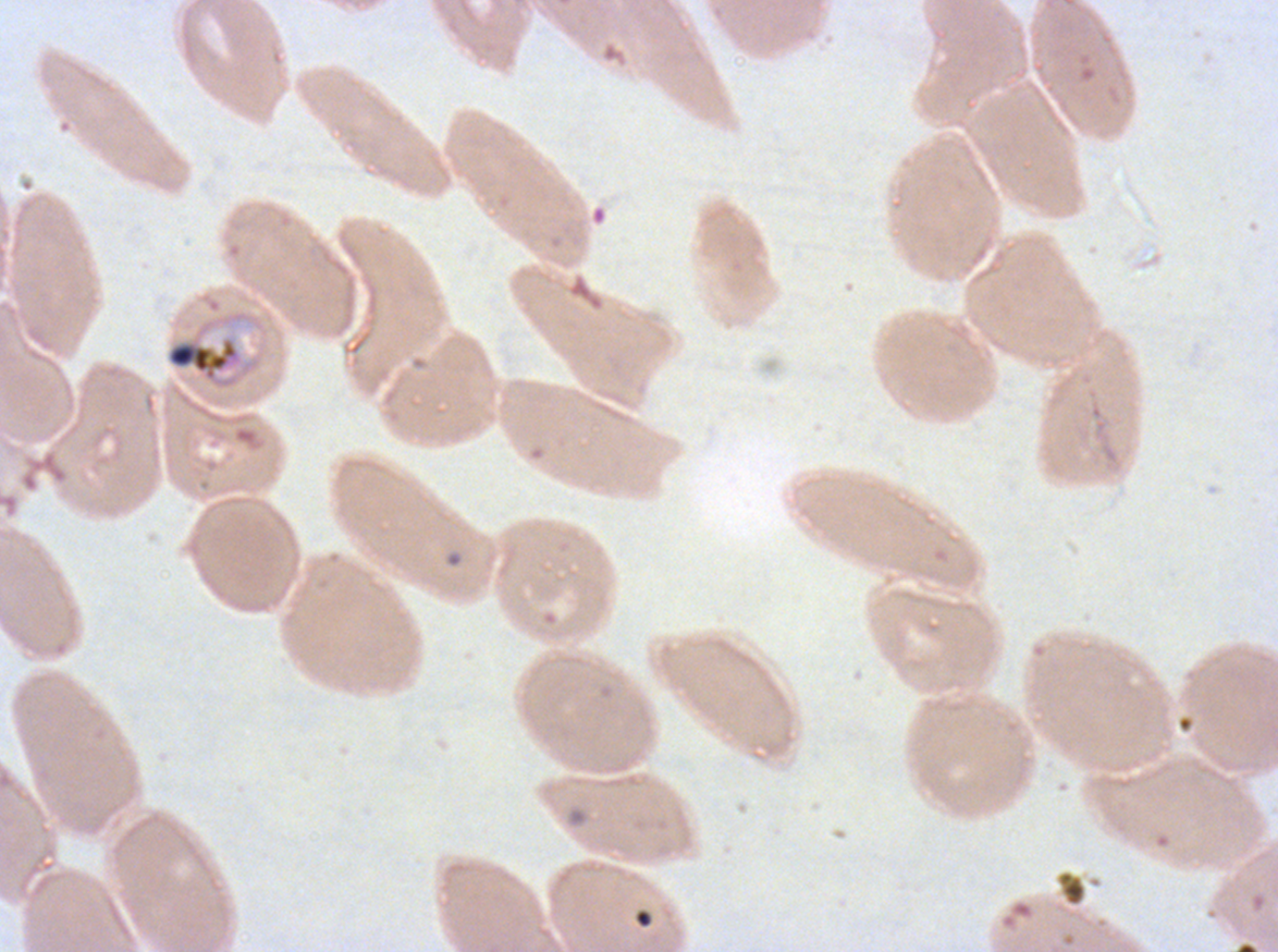
notation = approximate bounding boxes as {x1, y1, x2, y2} in pixels
mid trophozoite locations = {165, 309, 261, 391}
ring locations = {633, 909, 653, 929}
debris locations = {1056, 870, 1087, 907}
field of view = sub-image separated from a larger composite
image size = 1278×952 pixels
stain = Giemsa
specimen = ex-vivo P. falciparum culture from a patient in The Gambia, grown for 24 to 48 hours
life-cycle stages observed = ring, mid trophozoite
preparation = thin blood smear